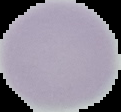
preparation = thin blood film
malaria status = uninfected
image type = segmented cell region on a black background
image size = 121×112 pixels